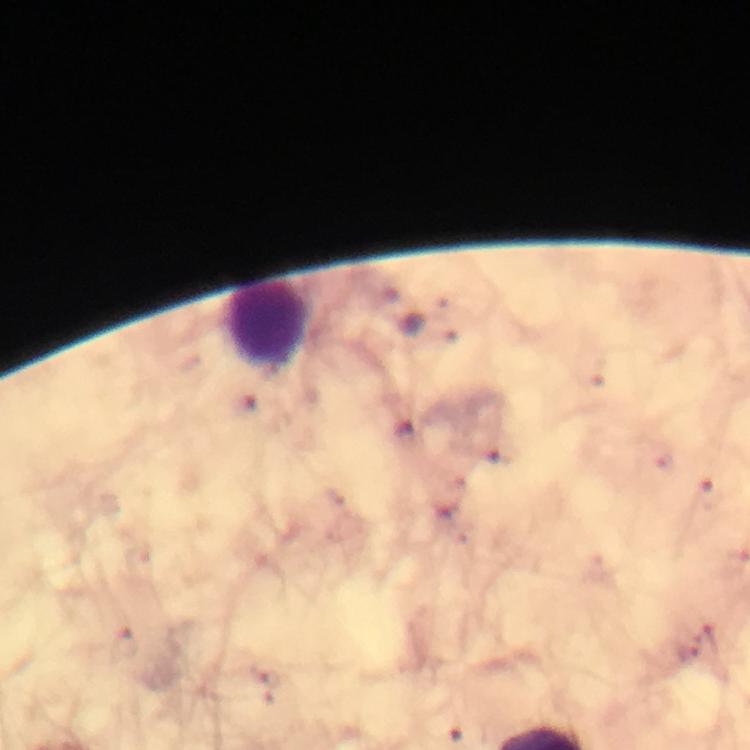
image_size: 750×750 pixels
preparation: thick blood film
leukocyte_locations: 'approximate centers as (x, y) in pixels: (270, 324)'
plasmodium_parasites: none seen
cropped_from: one field of view
magnification: 100x
stain: Giemsa
immersion_oil: used
capture: smartphone camera through the microscope
context: from a malaria diagnostic workup